Report the malaria status of this cell.
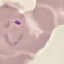
Parasitized.

Acquired by smartphone through the microscope eyepiece. Giemsa-stained preparation. Automatically extracted cell patch, resized to 64 × 64 pixels. Thin blood smear.